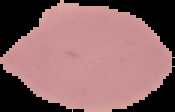

preparation: thin blood smear
result: no malaria parasites seen
image_type: segmented cell region on a black background
image_size: 175×112 pixels